State which parasite is depicted.
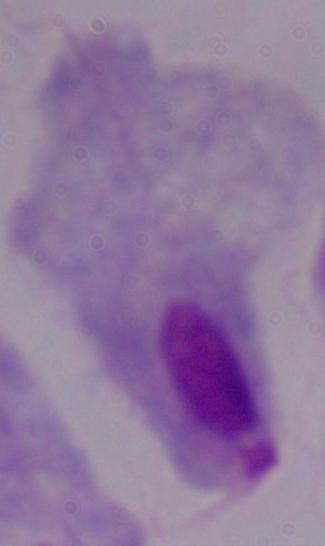

This is a trichomonad.

{
  "modality": "photomicrograph",
  "magnification": "1000x"
}